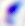
Summary:
  - Identification: Toxoplasma gondii
  - Magnification: 400x
  - Modality: photomicrograph